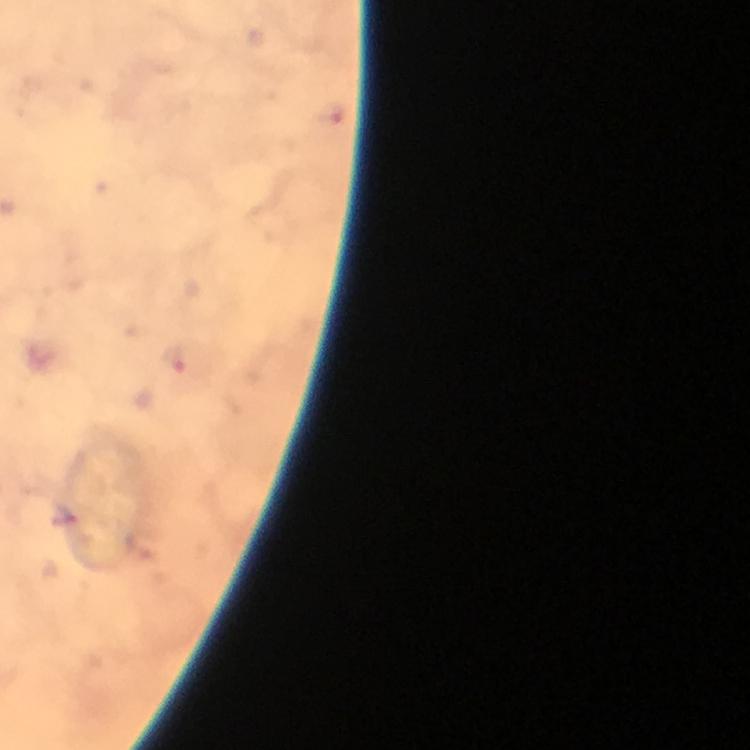

Approximate centers as {x, y} in pixels. Plasmodium parasite locations: {176, 363}. From a malaria diagnostic workup. Cropped region of a single field of view. Immersion oil applied. Image is 750×750 pixels. Thick blood film. Giemsa-stained preparation. 100x magnification. Photographed through the microscope with a smartphone camera.